Assess for Plasmodium parasites.
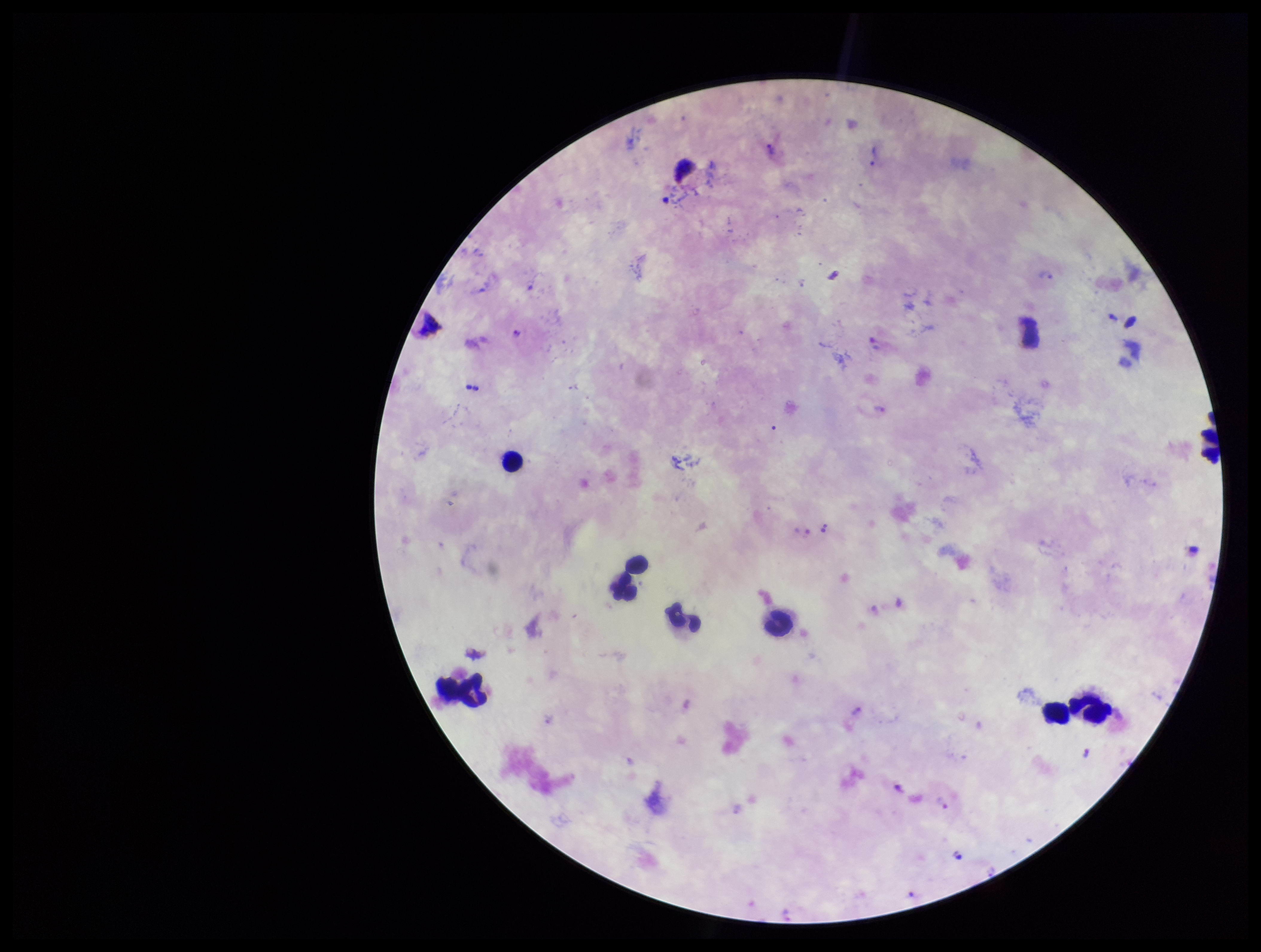

Identified.

{
  "leukocyte_count": 9,
  "image_size": "1261×952 pixels",
  "species_reported_for_this_patient": "Plasmodium vivax",
  "preparation": "thick smear",
  "capture": "smartphone photograph through the microscope eyepiece",
  "field_of_view": "single",
  "parasite_count": 8,
  "stain": "Giemsa",
  "patient_malaria_status": "infected"
}